Give the extent of all Plasmodium falciparum-infected red blood cells.
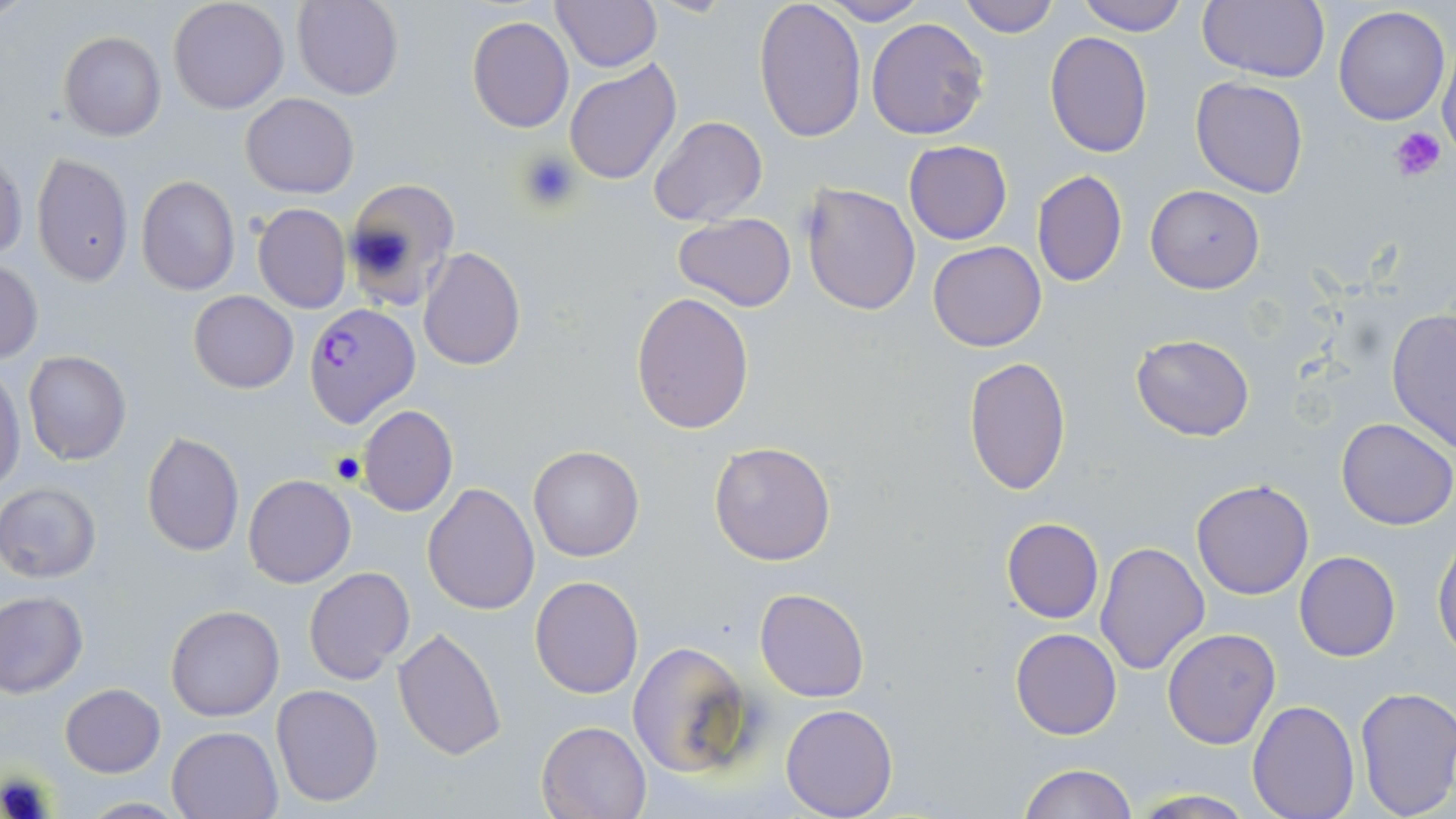
Approximate bounding boxes as (x1,y1)-(x2,y2) corner pairs in pixels.
Plasmodium falciparum-infected red blood cells: (303,302)-(420,429).

slide_level_diagnosis: Plasmodium falciparum
preparation: thin blood film
image_size: 1456×819 pixels
stain: May-Grünwald-Giemsa
field_of_view: single
modality: optical microscopy
uninfected_red_blood_cell_locations: 'approximate bounding boxes as (x1,y1)-(x2,y2) corner pairs in pixels: (168,0)-(289,114), (549,0)-(662,72), (754,0)-(866,143), (957,0)-(1061,38), (1198,0)-(1329,83), (291,1)-(405,100), (820,1)-(930,24), (1075,1)-(1189,37), (1332,6)-(1450,126), (468,15)-(574,133), (865,18)-(990,139), (59,31)-(167,141), (1045,33)-(1152,157), (1438,49)-(1456,157), (564,58)-(682,186), (1190,77)-(1310,199), (240,93)-(358,198), (649,115)-(768,227), (904,140)-(1012,244), (0,151)-(26,262), (31,152)-(133,286), (1030,170)-(1127,289), (136,174)-(240,295), (342,177)-(461,309), (1146,183)-(1265,294), (801,184)-(921,316), (252,203)-(352,313), (673,212)-(798,310), (928,240)-(1047,351), (417,247)-(526,370), (0,260)-(43,363), (188,290)-(298,393), (630,291)-(755,435), (1385,306)-(1456,452), (1131,333)-(1255,440), (22,350)-(132,467), (963,356)-(1072,496), (0,367)-(26,495), (357,405)-(458,517), (1336,417)-(1456,530), (141,431)-(244,556), (708,441)-(836,566), (528,445)-(644,562), (243,474)-(356,588), (1191,479)-(1314,601), (0,482)-(102,583), (422,482)-(540,615), (1001,517)-(1103,623), (1432,538)-(1456,657), (1094,541)-(1211,675), (1294,551)-(1400,661), (303,566)-(415,686), (530,574)-(644,699), (755,587)-(869,702), (0,590)-(88,697), (166,604)-(285,721), (392,625)-(506,760), (1010,628)-(1121,739), (1162,628)-(1282,749), (628,640)-(755,779), (270,683)-(384,807), (60,684)-(165,777), (1355,685)-(1456,819), (1247,700)-(1360,819), (781,703)-(898,818), (537,719)-(654,818), (166,724)-(284,818), (1016,763)-(1137,819), (1127,790)-(1261,819), (77,798)-(193,817)'
platelet_locations: 'approximate bounding boxes as (x1,y1)-(x2,y2) corner pairs in pixels: (1390,125)-(1447,179), (516,149)-(581,212)'
magnification: 1000x